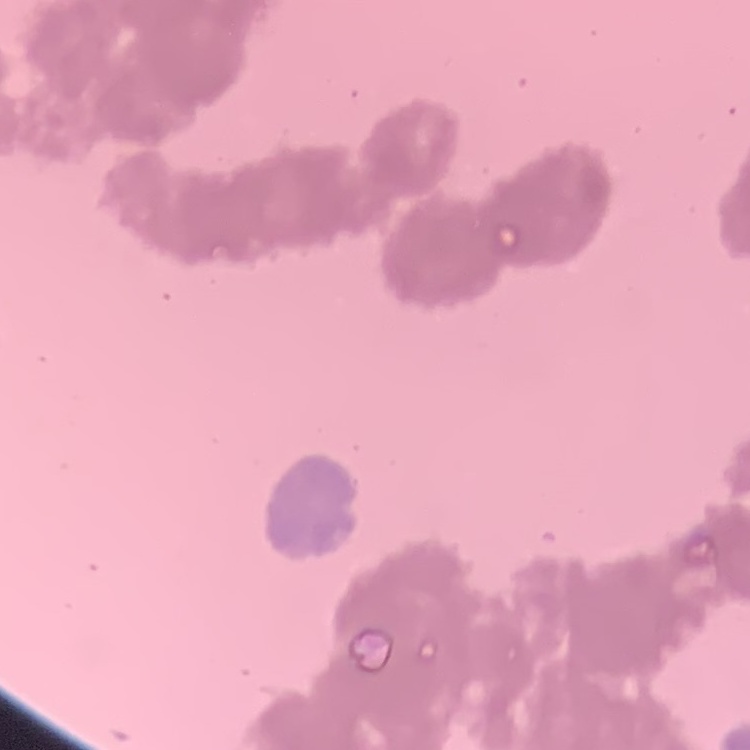 The erythrocytes exhibit rouleaux formation. Field's or Giemsa stain. Square crop of a larger photomicrograph. Thin blood film.